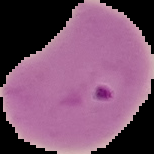

malaria status = parasitized
preparation = thin blood film
image size = 154×154 pixels
image type = segmented cell region on a black background